Point out every malaria parasite.
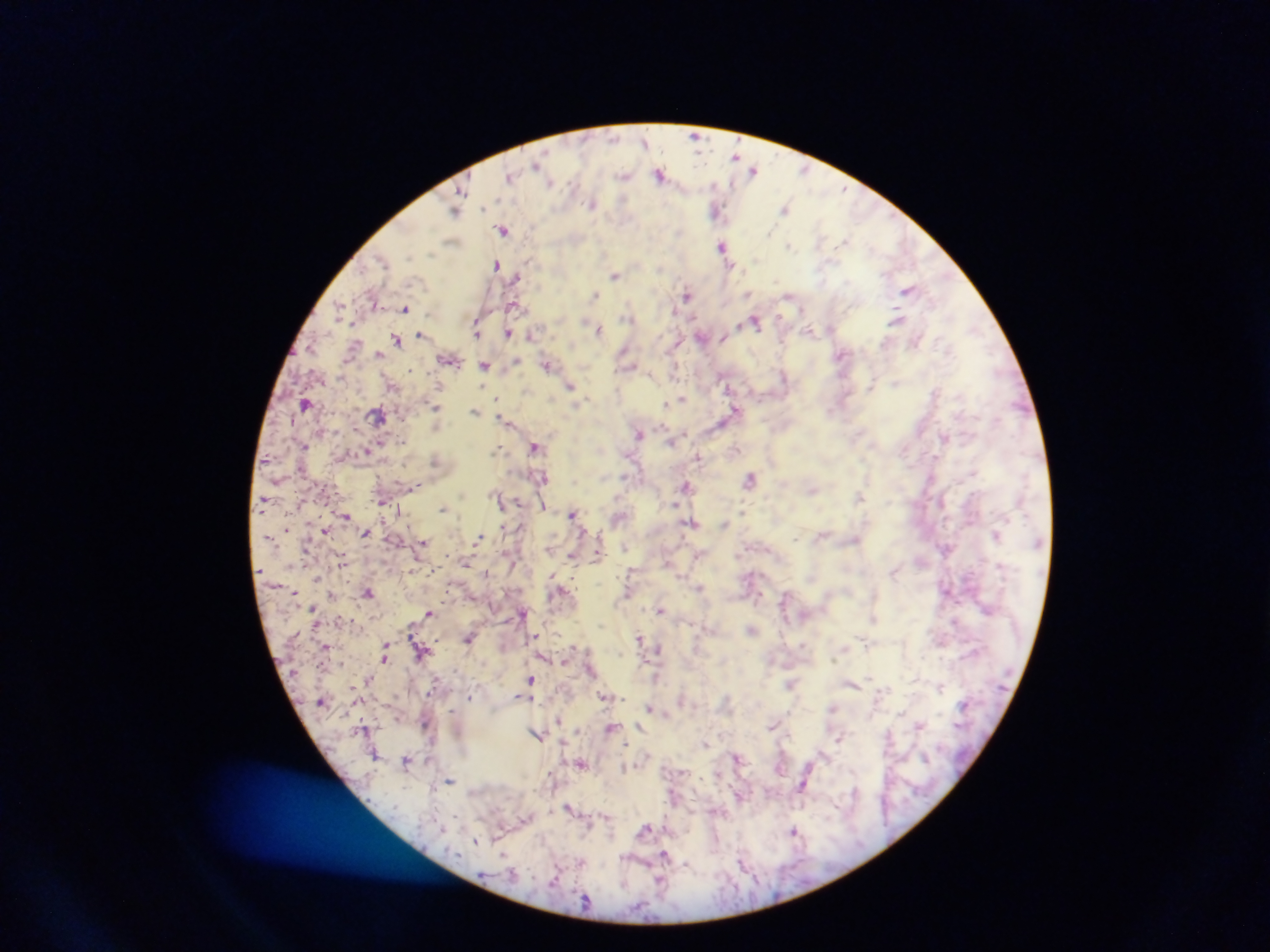
Approximate centers as [x, y] in pixels.
Malaria parasites: [410, 370], [529, 457], [573, 513], [287, 528].

capture = mobile-phone photograph through a microscope
field of view = single
preparation = thick blood film
country = Ghana
image size = 1270×952 pixels